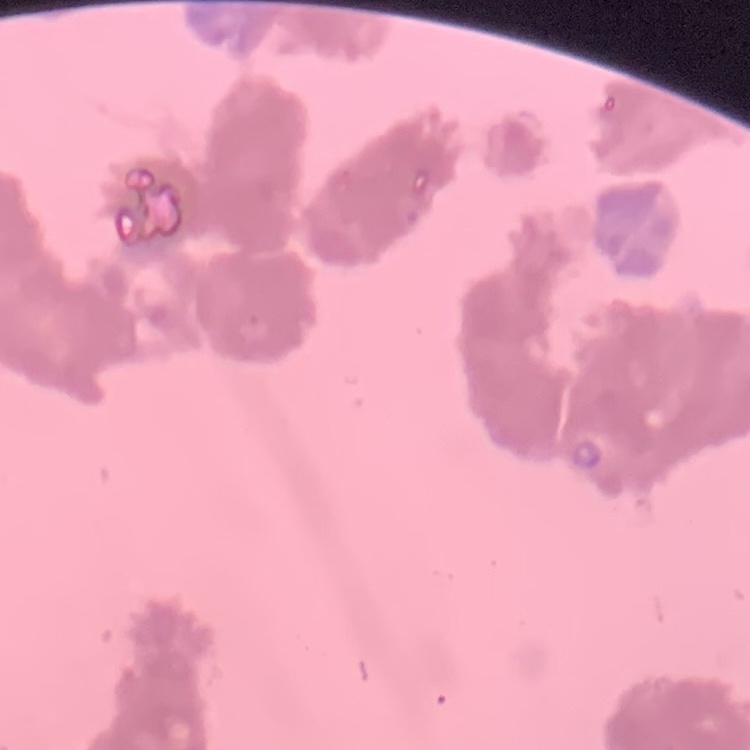
erythrocyte morphology = rouleaux formation
stain = Field's or Giemsa
image type = square crop of a larger photomicrograph
preparation = thin peripheral smear